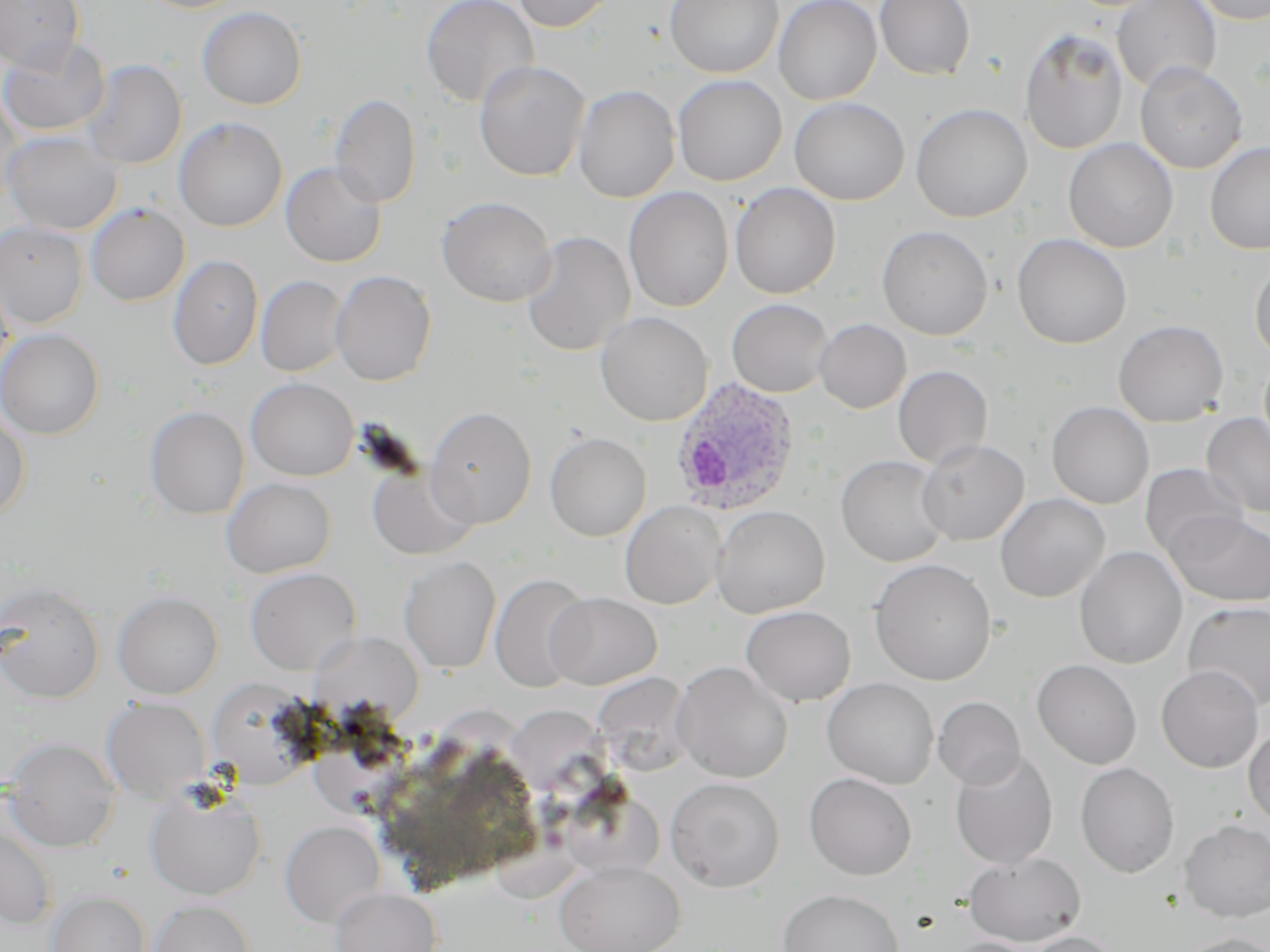
slide-level diagnosis = Plasmodium ovale
uninfected red blood cell locations = approximate bounding boxes as (x1, y1, x2, y2) in pixels: (0, 0, 84, 70), (420, 0, 539, 107), (511, 0, 617, 32), (665, 0, 784, 78), (773, 0, 882, 104), (875, 0, 975, 79), (1112, 0, 1221, 92), (1191, 0, 1270, 25), (197, 6, 307, 110), (1020, 29, 1128, 154), (0, 34, 109, 136), (82, 59, 186, 169), (474, 61, 590, 181), (1135, 61, 1247, 174), (673, 75, 787, 186), (574, 85, 680, 203), (0, 91, 23, 209), (329, 93, 421, 208), (789, 97, 909, 205), (910, 103, 1032, 223), (174, 116, 287, 232), (3, 131, 122, 235), (1063, 138, 1178, 252), (1204, 142, 1270, 255), (281, 162, 387, 267), (730, 182, 841, 299), (623, 186, 734, 312), (436, 196, 556, 306), (85, 203, 190, 306), (0, 221, 88, 328), (876, 225, 994, 340), (520, 231, 636, 356), (1012, 233, 1132, 349), (168, 254, 263, 371), (1249, 257, 1270, 363), (0, 270, 14, 386), (330, 270, 437, 386), (256, 275, 349, 377), (726, 298, 833, 397), (595, 311, 713, 426), (814, 318, 911, 413), (1113, 319, 1229, 426), (0, 329, 104, 439), (892, 365, 993, 469), (246, 377, 359, 481), (1047, 401, 1154, 509), (424, 405, 537, 528), (145, 406, 249, 519), (0, 409, 31, 520), (1201, 412, 1270, 518), (545, 432, 651, 541), (917, 439, 1029, 545), (836, 454, 951, 567), (1140, 463, 1246, 561), (367, 465, 477, 561), (222, 477, 336, 577), (995, 493, 1110, 602), (620, 500, 726, 609), (711, 505, 830, 618), (1166, 511, 1270, 607), (1074, 546, 1187, 668), (399, 556, 502, 674), (869, 558, 996, 685), (244, 567, 361, 676), (489, 573, 592, 692), (0, 581, 105, 704), (112, 591, 223, 698), (546, 592, 662, 689), (1183, 600, 1270, 712), (741, 606, 856, 705), (311, 630, 424, 719), (1032, 659, 1141, 769), (672, 661, 793, 783), (1156, 665, 1264, 772), (592, 672, 696, 775), (822, 678, 939, 788), (933, 696, 1025, 789), (102, 697, 211, 802), (1243, 726, 1270, 826), (3, 737, 121, 852), (949, 749, 1058, 869), (1075, 763, 1180, 878), (803, 772, 916, 880), (665, 777, 785, 892), (145, 787, 266, 900), (1180, 820, 1270, 921), (280, 821, 385, 928), (0, 826, 57, 929), (963, 852, 1086, 945), (554, 861, 684, 952), (330, 888, 441, 952), (777, 888, 904, 952), (46, 891, 151, 952), (147, 900, 256, 952), (1022, 931, 1122, 952), (1174, 933, 1270, 952), (943, 938, 1040, 952)
preparation = thin blood film
stain = May-Grünwald-Giemsa
image size = 1270×952 pixels
Plasmodium ovale-infected red blood cell locations = approximate bounding boxes as (x1, y1, x2, y2) in pixels: (670, 377, 800, 517)
field of view = one of a larger specimen
magnification = 1000x
modality = optical microscopy